Assess this cell for malaria.
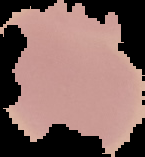
Uninfected.

image size = 145×157 pixels
image type = segmented cell region on a black background
preparation = thin blood film